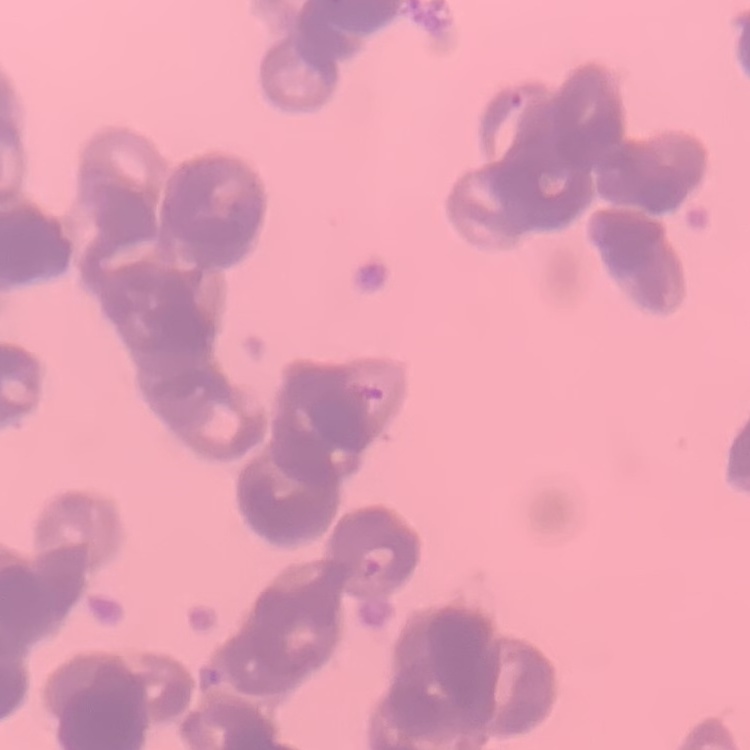 The erythrocytes exhibit rouleaux formation. Square crop of a larger photomicrograph. Thin peripheral smear. Stained with either Field's or Giemsa.